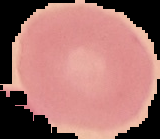 Malaria status: uninfected. Image is 160×139 pixels. Segmented cell region on a black background. From a thin blood smear.